State which parasite is depicted.
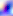

This is Toxoplasma gondii.

Captured at 400x magnification. Micrograph.